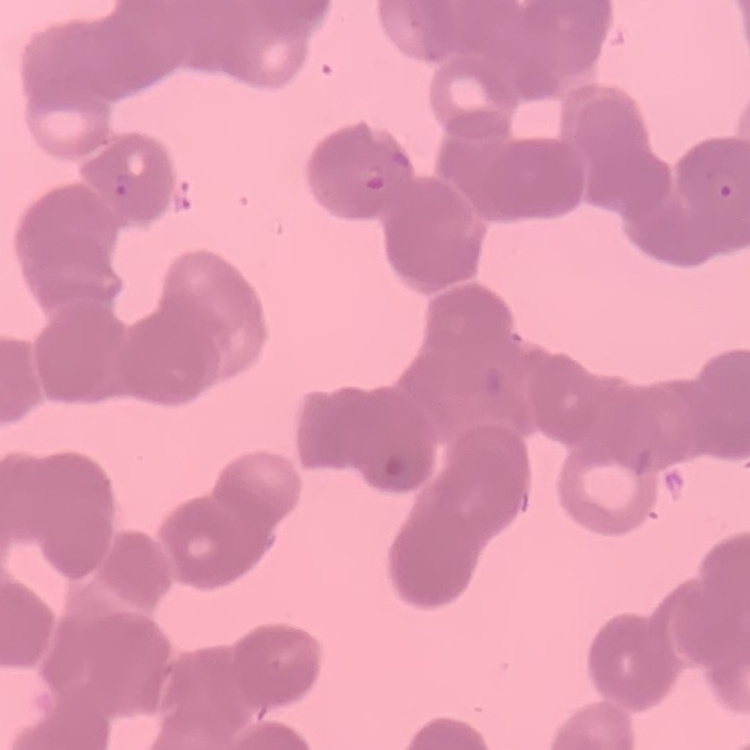

Summary:
  - Red blood cell morphology: rouleaux formation
  - Preparation: thin blood smear
  - Image type: one tile cut from a larger photomicrograph
  - Stain: Field's or Giemsa